Point out every malaria parasite and every leukocyte.
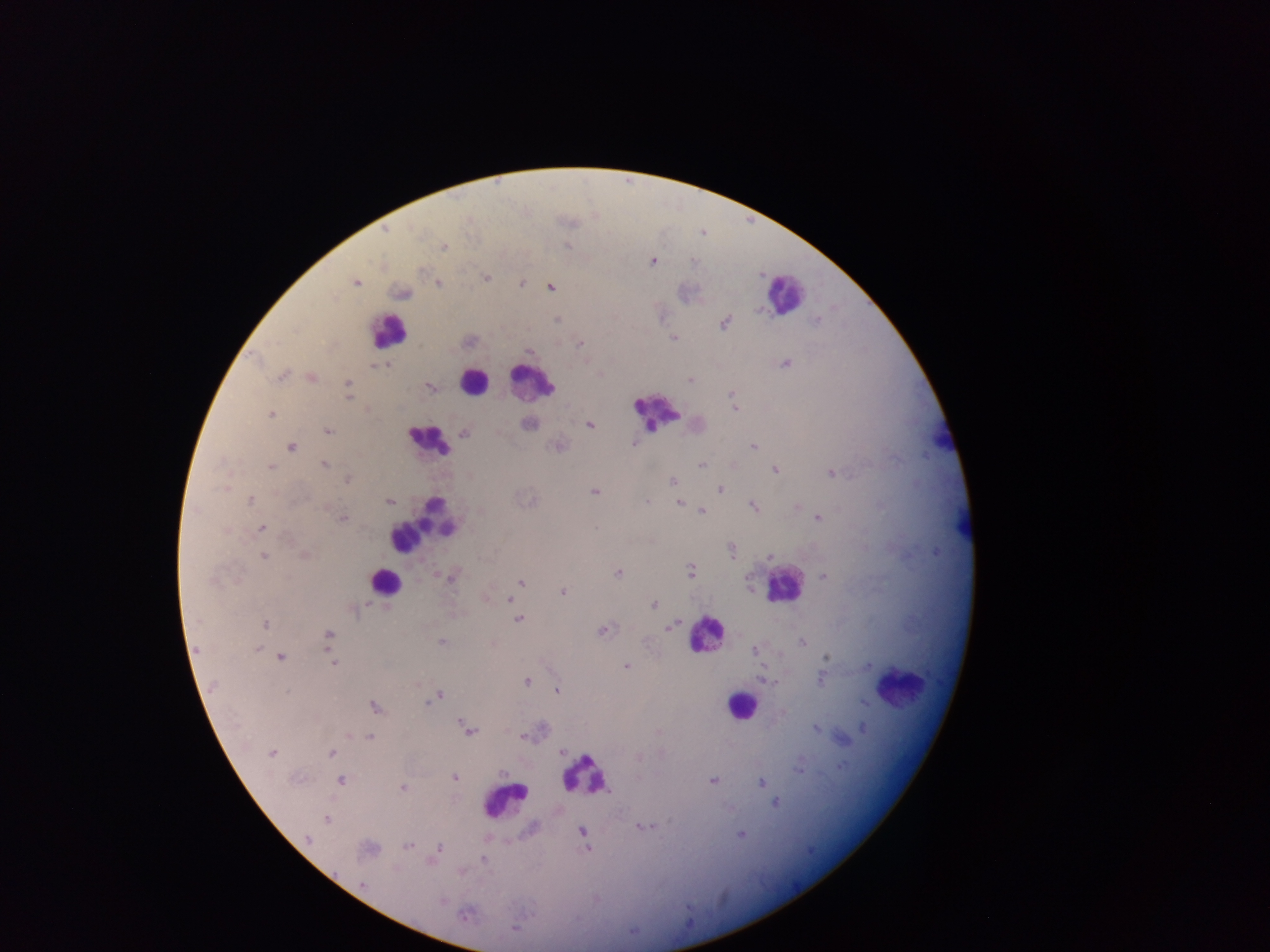
Approximate centers as x y in pixels.
Malaria parasites: 385 230; 443 247; 651 260; 486 278; 355 282; 438 283; 520 283; 550 287; 402 293; 558 319; 725 323; 674 337; 580 344; 529 350; 785 363; 384 364; 281 376; 310 378; 690 379; 348 384; 429 388; 348 394; 732 394; 734 408; 270 414; 528 423; 590 424; 328 430; 464 432; 496 433; 631 443; 558 445; 753 446; 290 447; 323 465; 702 465; 735 465; 270 467; 774 470; 831 472; 346 479; 671 482; 719 488; 594 491; 250 500; 389 500; 645 502; 678 502; 797 506; 754 507; 701 512; 342 518; 818 518; 262 528; 731 552; 305 555; 264 556; 769 556; 691 570; 618 573; 451 576; 823 576; 521 583; 562 591; 485 597; 509 599; 653 603; 519 619; 265 625; 669 627; 601 629; 328 637; 441 642; 803 643; 256 647; 755 650; 281 657; 825 657; 334 662; 626 666; 821 677; 762 679; 527 681; 211 687; 556 690; 439 695; 862 701; 425 702; 374 707; 782 712; 461 720; 816 727; 373 728; 863 728; 469 730; 523 735; 369 736; 560 751; 271 752; 331 753; 839 767; 454 777; 340 780; 712 780; 762 783; 402 787; 774 802; 327 819; 642 826; 582 831; 741 834; 306 838; 408 845; 439 847; 588 848; 368 849; 483 859; 362 885; 441 902; 464 915.
Leukocytes: 783 293; 388 331; 530 381; 473 382; 655 412; 428 439; 423 523; 384 583; 783 584; 706 634; 900 688; 742 706; 584 775; 504 801.

capture = mobile-phone photograph through a microscope
country = Ghana
image size = 1270×952 pixels
field of view = single
preparation = thick blood film